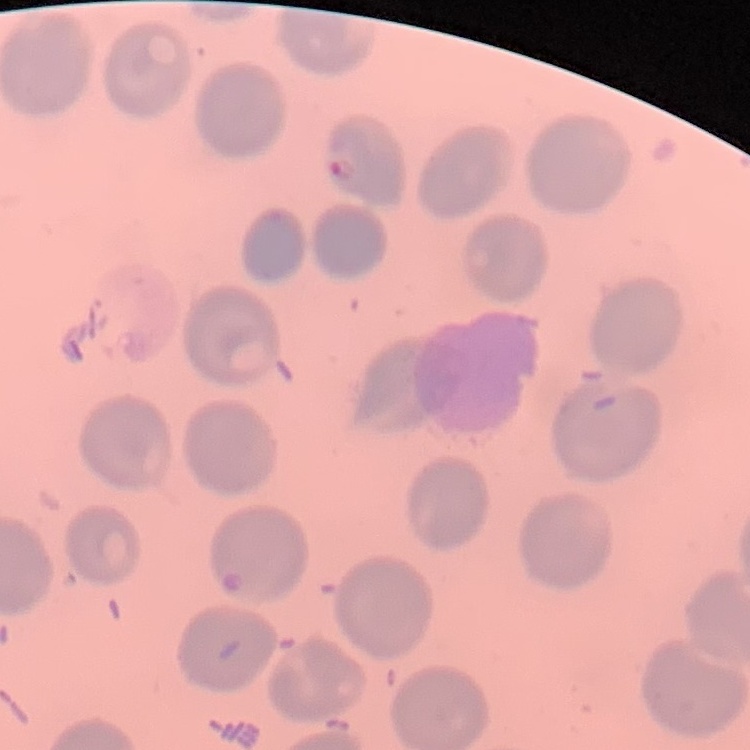
The red blood cells show no rouleaux formation. One tile cut from a larger photomicrograph. Thin peripheral smear. Field's or Giemsa stain.